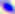
Captured at 400x magnification. Photomicrograph. Toxoplasma gondii is shown.